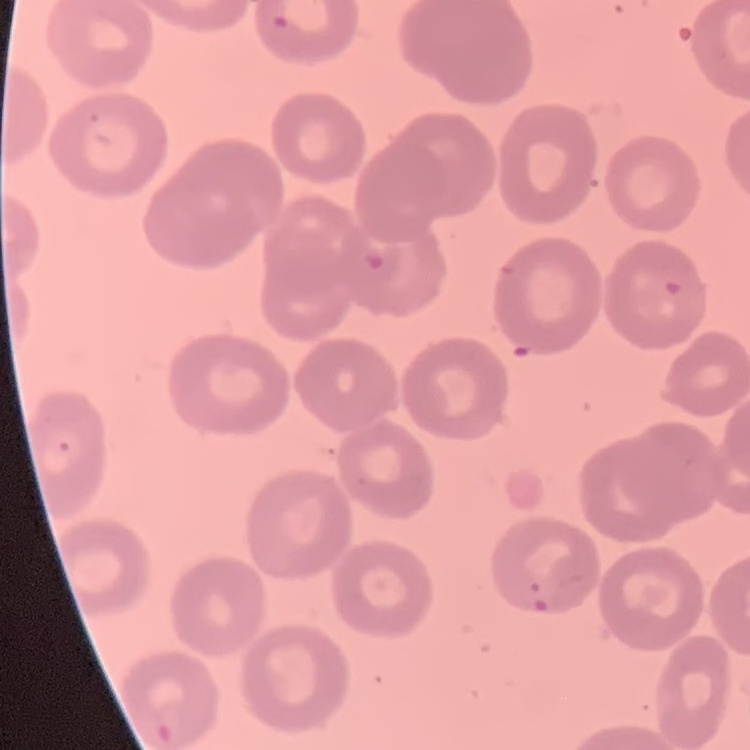
Summary:
  - Red blood cell morphology: no rouleaux formation
  - Stain: Field's or Giemsa
  - Preparation: thin blood smear
  - Image type: one tile cut from a larger photomicrograph